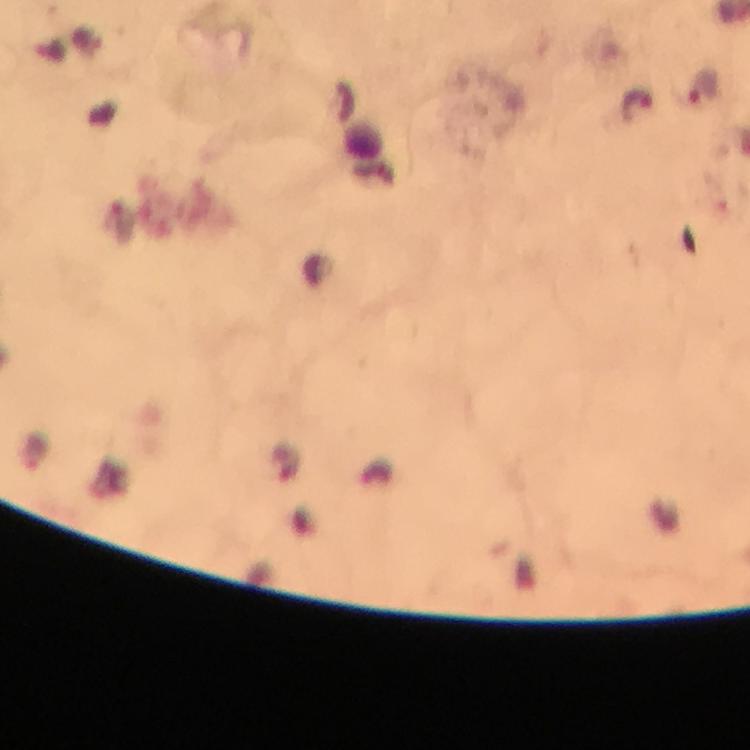

Approximate object centers, in pixels from the top-left corner.
Summary:
  - Plasmodium parasite locations: (x=704, y=88), (x=638, y=106)
  - Capture: smartphone mounted on the microscope
  - Cropped from: a single field of view
  - Immersion oil: applied
  - Stain: Giemsa
  - Preparation: thick blood smear
  - Context: from a malaria diagnostic workup
  - Image size: 750×750 pixels
  - Magnification: 100x